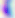
Summary:
  - Identification: Toxoplasma gondii
  - Magnification: 400x
  - Modality: photomicrograph